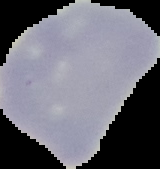

{
  "image_size": "160×169 pixels",
  "image_type": "segmented cell region on a black background",
  "preparation": "thin blood smear",
  "result": "negative for malaria parasites"
}